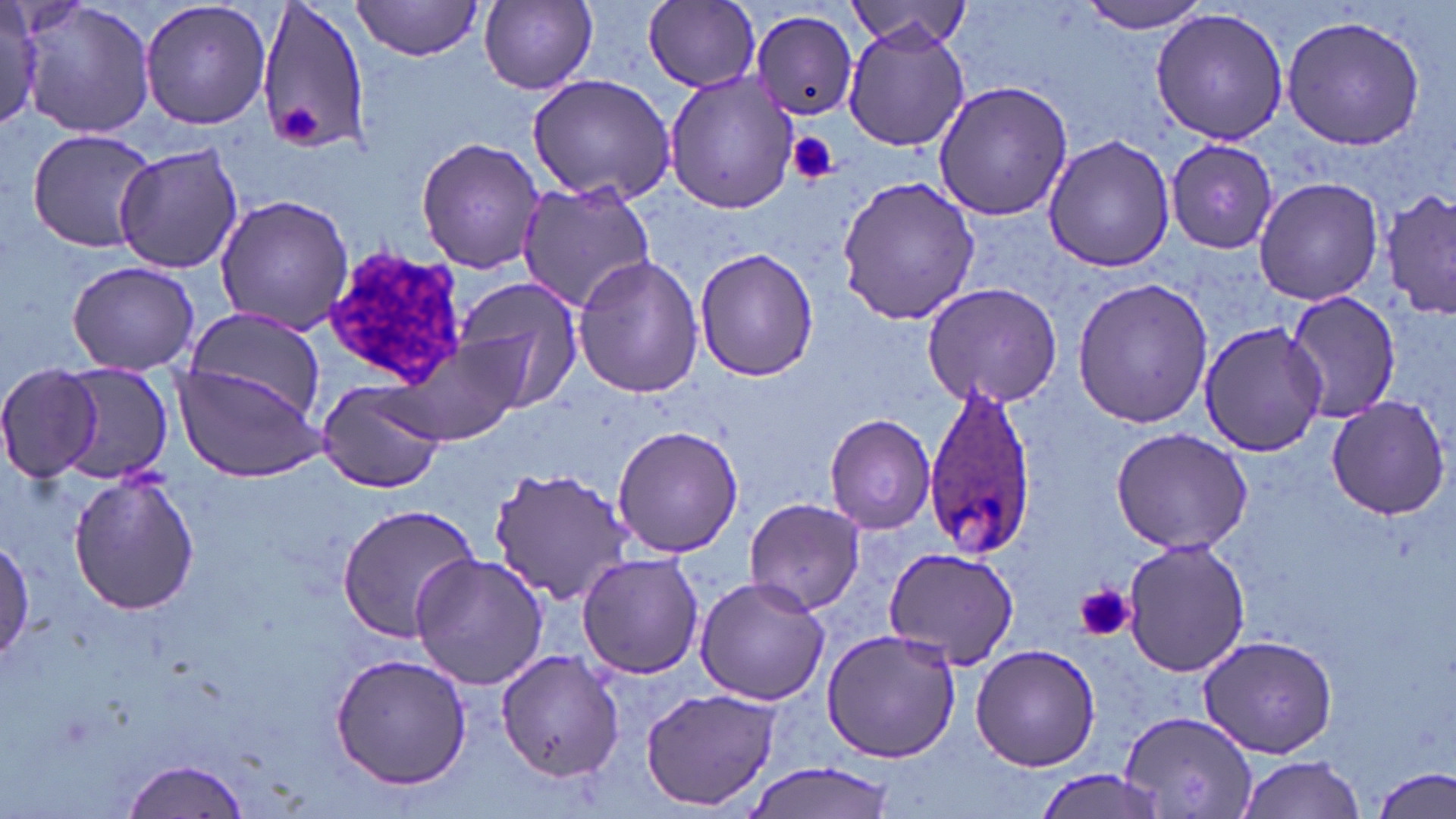

Summary:
  - Coordinate format: approximate bounding boxes as (x1, y1, x2, y2) in pixels
  - Uninfected red blood cell locations: (19, 0, 157, 142), (140, 0, 273, 130), (256, 0, 371, 156), (351, 0, 484, 60), (845, 0, 976, 50), (1079, 0, 1213, 36), (478, 1, 597, 92), (643, 1, 759, 91), (0, 4, 43, 128), (1149, 7, 1290, 144), (750, 8, 859, 120), (1280, 13, 1428, 151), (842, 23, 969, 153), (661, 70, 804, 214), (527, 73, 678, 205), (932, 81, 1074, 222), (26, 130, 157, 251), (1043, 132, 1174, 273), (416, 136, 547, 274), (1165, 138, 1280, 256), (113, 142, 243, 275), (836, 174, 981, 327), (1252, 176, 1386, 306), (517, 180, 659, 313), (1382, 187, 1456, 322), (213, 195, 357, 335), (694, 246, 821, 380), (571, 254, 704, 400), (66, 259, 200, 376), (1070, 276, 1213, 428), (452, 278, 584, 409), (921, 280, 1063, 409), (1282, 287, 1401, 428), (181, 305, 331, 429), (1200, 319, 1326, 456), (402, 334, 530, 446), (0, 362, 110, 482), (44, 362, 176, 483), (173, 364, 325, 482), (316, 379, 448, 493), (1324, 394, 1451, 520), (823, 413, 937, 535), (611, 424, 744, 559), (1109, 429, 1253, 555), (484, 466, 636, 607), (68, 471, 200, 617), (743, 496, 866, 616), (337, 504, 481, 641), (1120, 536, 1249, 677), (0, 537, 33, 665), (882, 546, 1022, 671), (409, 551, 552, 690), (576, 552, 703, 680), (694, 575, 830, 707), (821, 627, 960, 762), (1197, 634, 1338, 757), (970, 644, 1100, 773), (492, 649, 626, 783), (330, 652, 473, 791), (640, 689, 782, 809), (1119, 713, 1257, 818), (1232, 753, 1366, 819), (122, 757, 252, 819), (742, 761, 900, 819), (1374, 764, 1455, 818), (1036, 768, 1170, 817)
  - Plasmodium ovale-infected red blood cell locations: (922, 378, 1037, 562)
  - Platelet locations: (279, 105, 320, 140), (787, 133, 839, 185), (1077, 583, 1135, 643)
  - White blood cell locations: (321, 245, 468, 397)
  - Slide-level diagnosis: Plasmodium ovale
  - Modality: light microscopy
  - Field of view: one of a larger specimen
  - Preparation: thin blood film
  - Stain: May-Grünwald-Giemsa
  - Image size: 1456×819 pixels
  - Magnification: 1000x